Assess the morphology of the red blood cells.
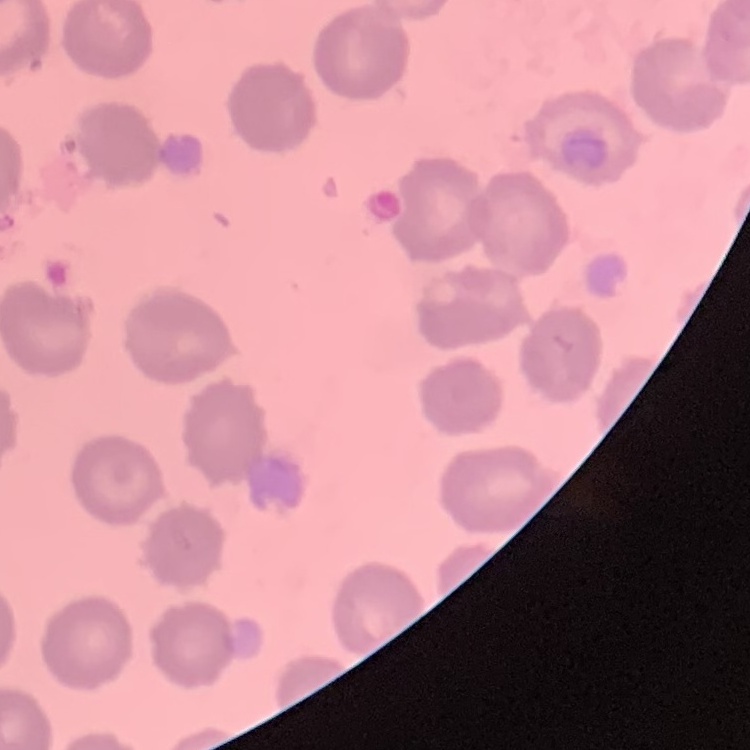
No rouleaux formation.

Thin blood smear. Square crop of a larger photomicrograph. Field's or Giemsa stain.